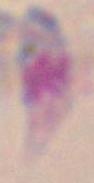 Toxoplasma gondii is seen. Micrograph. 1000x magnification.